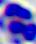

Summary:
  - Identification: white blood cell
  - Magnification: 400x
  - Modality: photomicrograph